State which parasite is depicted.
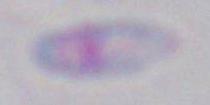
Toxoplasma gondii.

Summary:
  - Magnification: 1000x
  - Modality: photomicrograph